Comment on the morphology of the red blood cells.
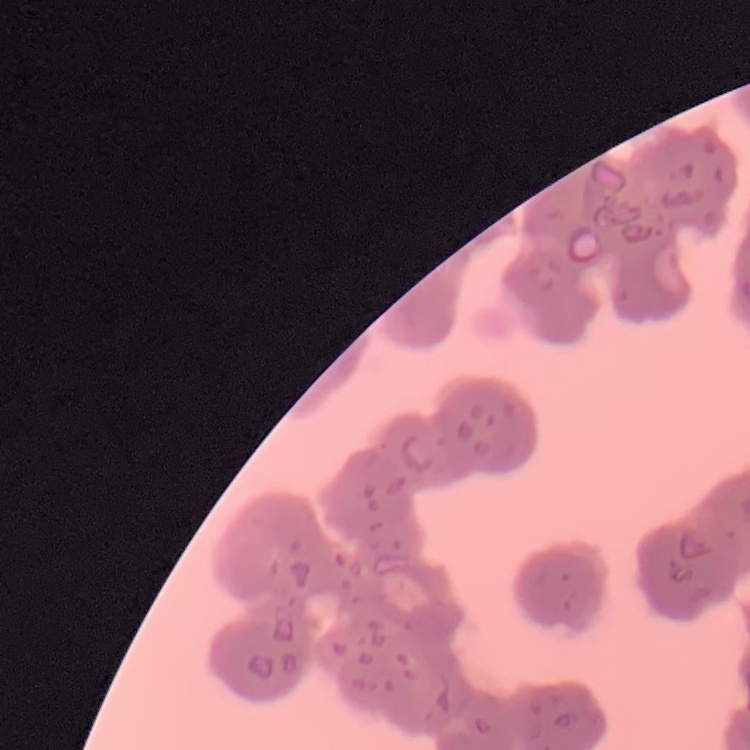
Rouleaux formation.

image type = square crop of a larger photomicrograph
preparation = thin blood film
stain = Field's or Giemsa